Report the malaria status of this cell.
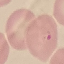

It is parasitized.

Photographed with a smartphone camera at the microscope eyepiece. Giemsa stain. Thin smear of blood. Automatically extracted cell patch, resized to 64 × 64 pixels.